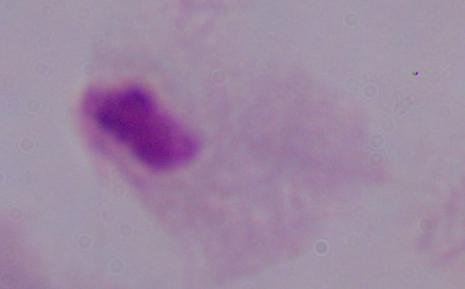
Summary:
  - Modality: micrograph
  - Identification: trichomonad
  - Magnification: 1000x